Give the preparation type.
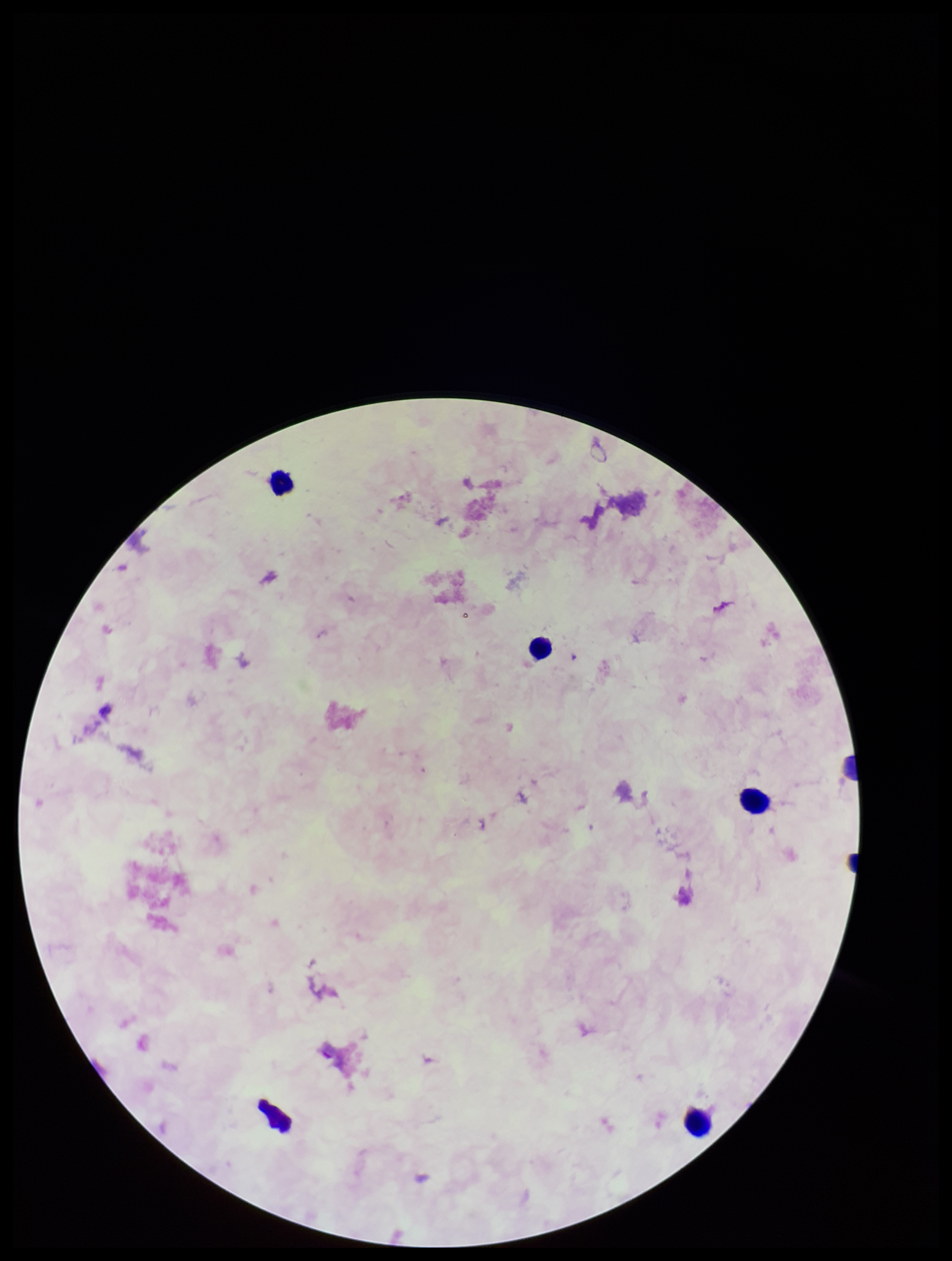
Thick.

Leukocyte count: 4. Patient malaria status: negative. Parasite count: 0. Single field of view. Giemsa stain. Smartphone photograph taken through the eyepiece of a microscope. Image is 952×1261 pixels. Plasmodium parasites: none identified.